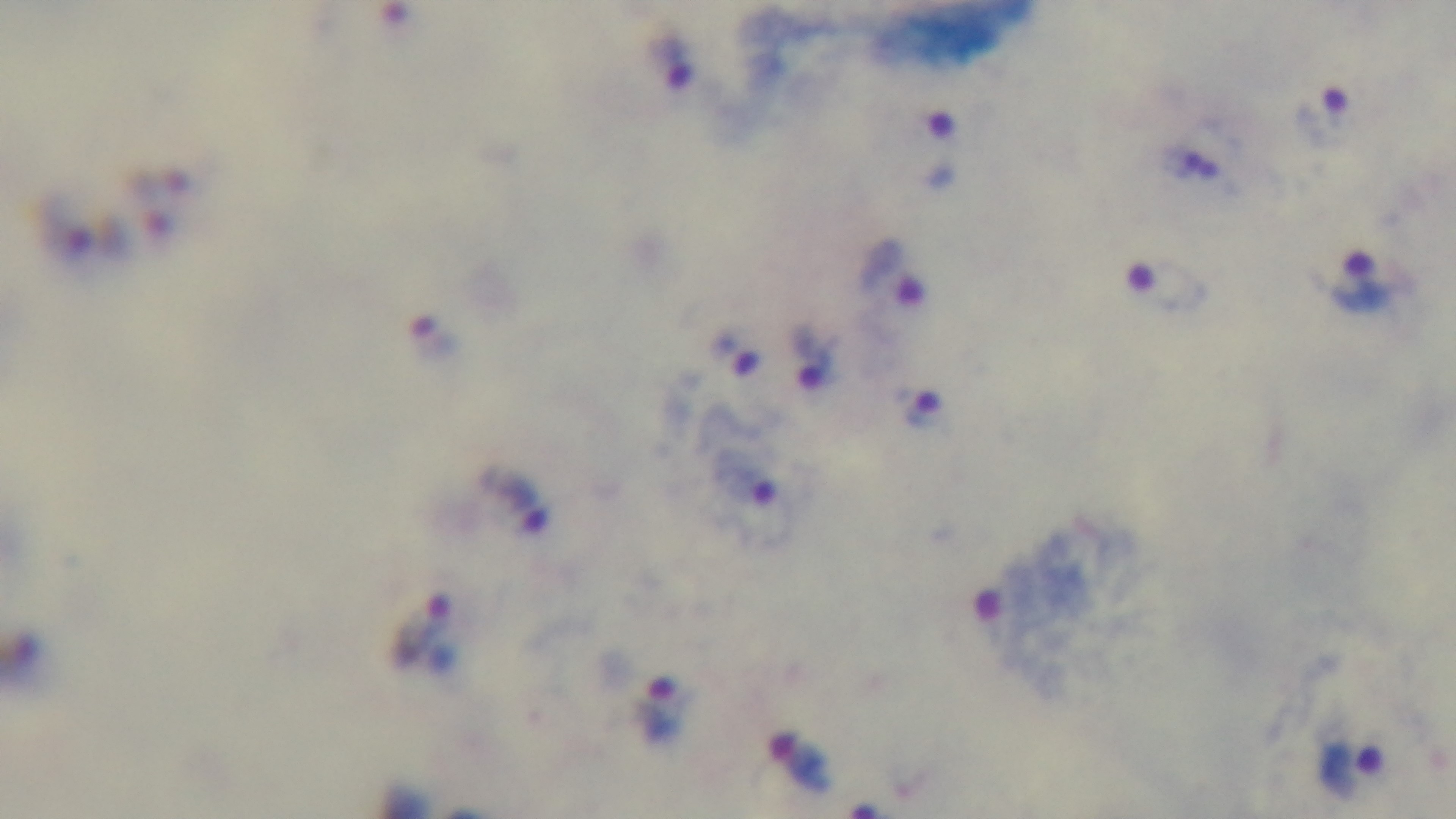

Malaria status: positive. Captured with a mounted 4K digital camera. One field from the slide. Giemsa stain. Photomicrograph. Preparation: thick. Oil-immersion objective, 100x.